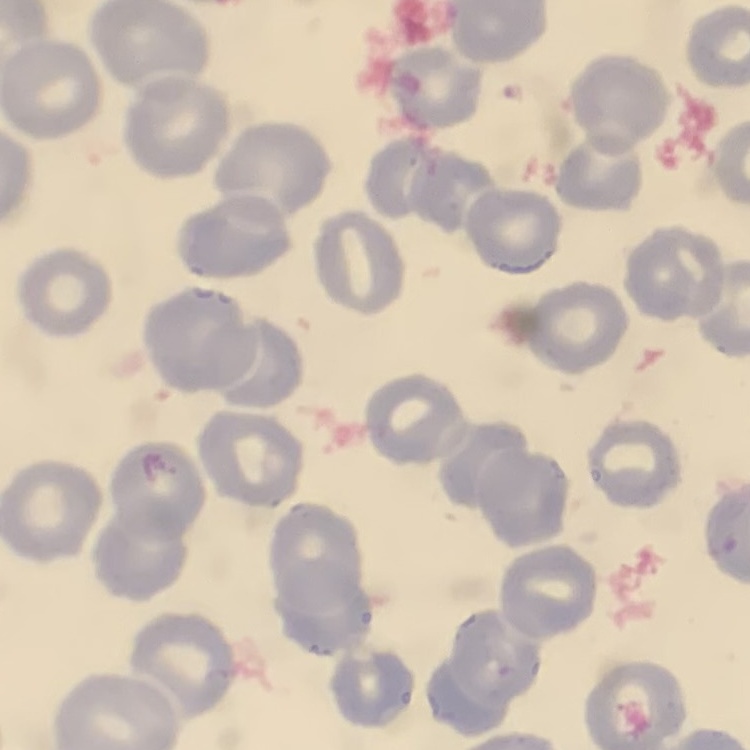
Summary:
  - Erythrocyte morphology: no rouleaux formation
  - Image type: square crop of a larger photomicrograph
  - Stain: Field's or Giemsa
  - Preparation: thin blood smear